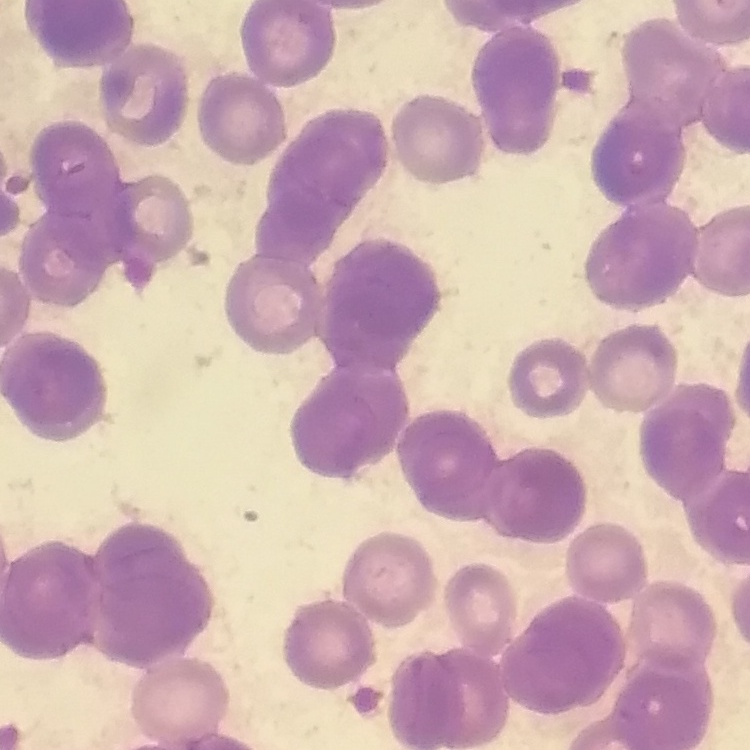

The erythrocytes exhibit rouleaux formation. Square crop of a larger photomicrograph. Stained with either Field's or Giemsa. Thin blood film.